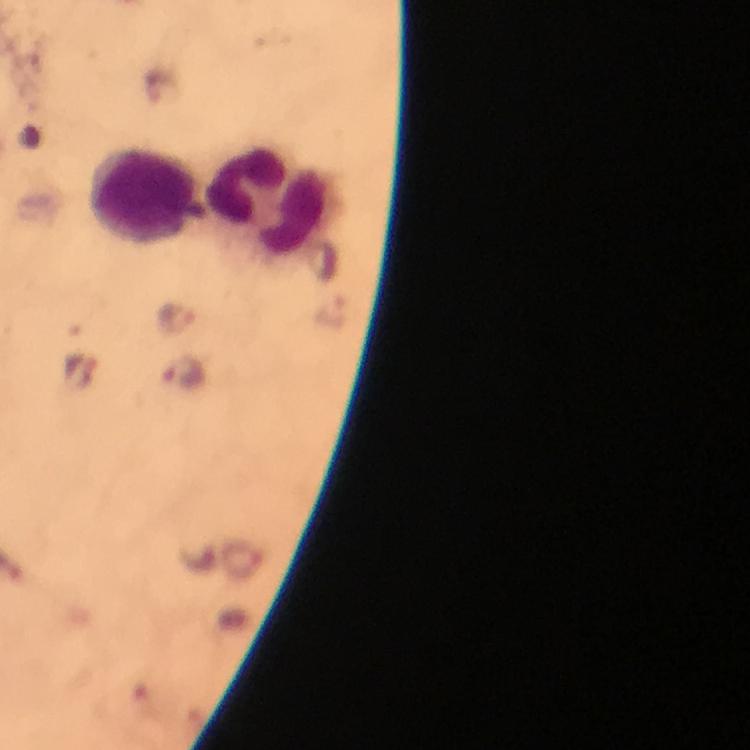

immersion oil = applied
capture = smartphone camera through the microscope
Plasmodium parasite locations = approximate object centers, in pixels from the top-left corner: (x=333, y=312), (x=177, y=319), (x=186, y=372)
image size = 750×750 pixels
preparation = thick smear
context = from a diagnostic examination for malaria
stain = Giemsa
leukocyte locations = approximate object centers, in pixels from the top-left corner: (x=143, y=194), (x=271, y=203)
cropped from = one field of view
magnification = 100x